Locate every blood parasite and identify its species.
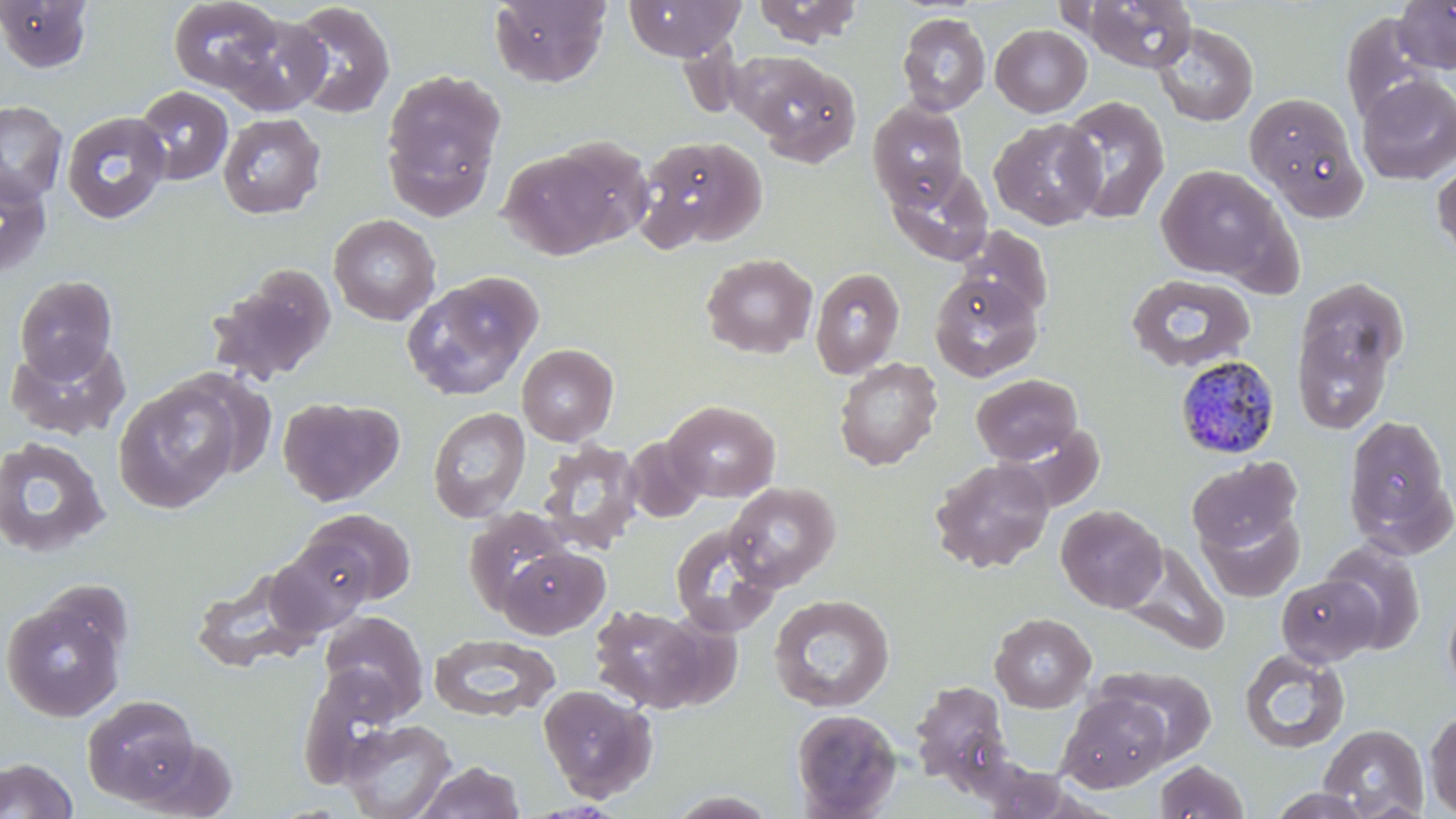
Approximate bounding boxes as (x1, y1, x2, y2) in pixels.
Plasmodium malariae-infected red blood cells: (1175, 356, 1281, 459).
No Plasmodium falciparum, Plasmodium ovale, Plasmodium vivax, Babesia divergens, or Trypanosoma brucei observed.

Summary:
  - Uninfected red blood cell locations: (489, 0, 611, 87), (624, 0, 745, 60), (753, 0, 864, 47), (1393, 0, 1456, 72), (0, 1, 94, 74), (167, 1, 284, 94), (1079, 1, 1197, 72), (285, 2, 395, 119), (896, 13, 991, 115), (212, 14, 331, 117), (1341, 14, 1437, 124), (1153, 23, 1258, 127), (990, 24, 1092, 117), (738, 53, 862, 165), (380, 67, 506, 220), (1356, 74, 1456, 185), (133, 85, 233, 185), (1245, 92, 1367, 218), (1057, 95, 1170, 224), (0, 100, 68, 206), (868, 100, 969, 208), (61, 111, 171, 224), (217, 113, 325, 218), (989, 118, 1105, 230), (634, 135, 767, 251), (500, 145, 628, 260), (1431, 159, 1456, 261), (885, 163, 994, 266), (1155, 164, 1291, 284), (0, 167, 53, 279), (329, 214, 440, 325), (960, 226, 1054, 322), (701, 253, 817, 359), (810, 266, 905, 379), (207, 267, 335, 385), (929, 272, 1043, 382), (1126, 272, 1257, 374), (401, 273, 543, 401), (15, 275, 118, 380), (1291, 282, 1407, 433), (5, 336, 130, 441), (517, 344, 619, 445), (833, 357, 943, 470), (970, 374, 1083, 465), (113, 379, 243, 513), (277, 396, 404, 507), (664, 400, 780, 502), (427, 407, 531, 523), (1342, 413, 1454, 550), (624, 435, 707, 523), (0, 436, 111, 558), (536, 439, 645, 554), (930, 457, 1055, 573), (1186, 457, 1301, 554), (724, 482, 840, 591), (1056, 504, 1166, 612), (1198, 506, 1305, 602), (300, 508, 417, 606), (463, 508, 575, 616), (669, 522, 782, 636), (265, 539, 373, 638), (1320, 540, 1427, 654), (1121, 543, 1230, 654), (498, 545, 609, 639), (190, 564, 324, 674), (1276, 575, 1381, 666), (1443, 591, 1456, 702), (1, 593, 128, 722), (768, 594, 896, 712), (588, 603, 722, 714), (319, 611, 429, 718), (989, 613, 1096, 712), (429, 633, 559, 722), (1239, 648, 1350, 753), (296, 664, 408, 787), (1100, 665, 1218, 764), (909, 680, 1014, 791), (537, 684, 657, 802), (1059, 691, 1170, 791), (82, 695, 201, 806), (790, 708, 902, 819), (1424, 709, 1456, 816), (338, 718, 458, 819), (1318, 724, 1429, 818), (0, 758, 78, 818), (1154, 759, 1249, 818), (415, 761, 525, 818), (1265, 788, 1377, 818), (665, 790, 781, 818)
  - Slide-level diagnosis: Plasmodium malariae
  - Magnification: 1000x
  - Field of view: one of a larger specimen
  - Image size: 1456×819 pixels
  - Modality: optical microscopy
  - Stain: May-Grünwald-Giemsa
  - Preparation: thin blood smear